Classify this cell by malaria status.
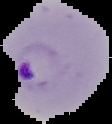
It is parasitized.

Summary:
  - Image type: cell region segmented out of the field of view; surrounding area masked to black
  - Image size: 112×124 pixels
  - Preparation: thin blood smear